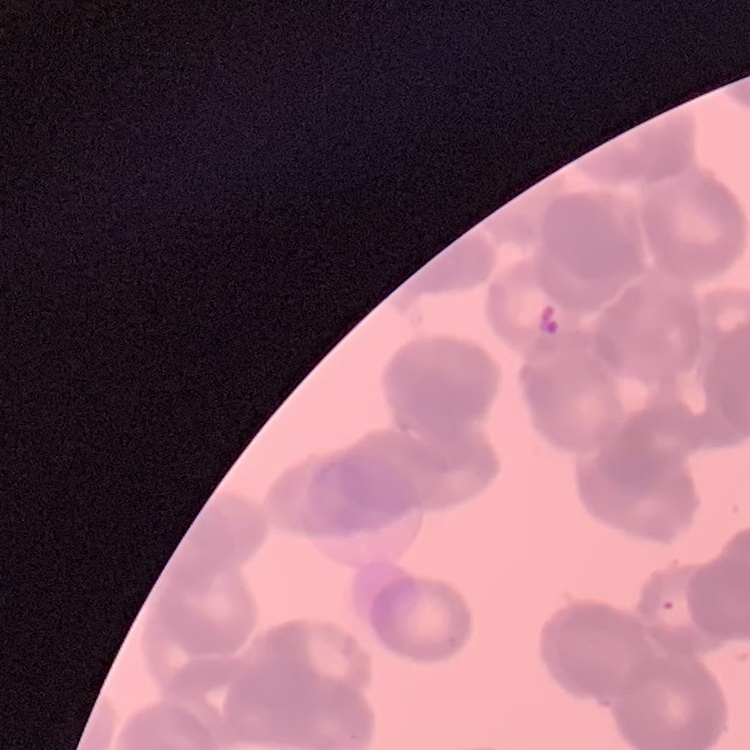

The red blood cells show rouleaux formation. Thin blood smear. Square crop of a larger photomicrograph. Field's or Giemsa stain.